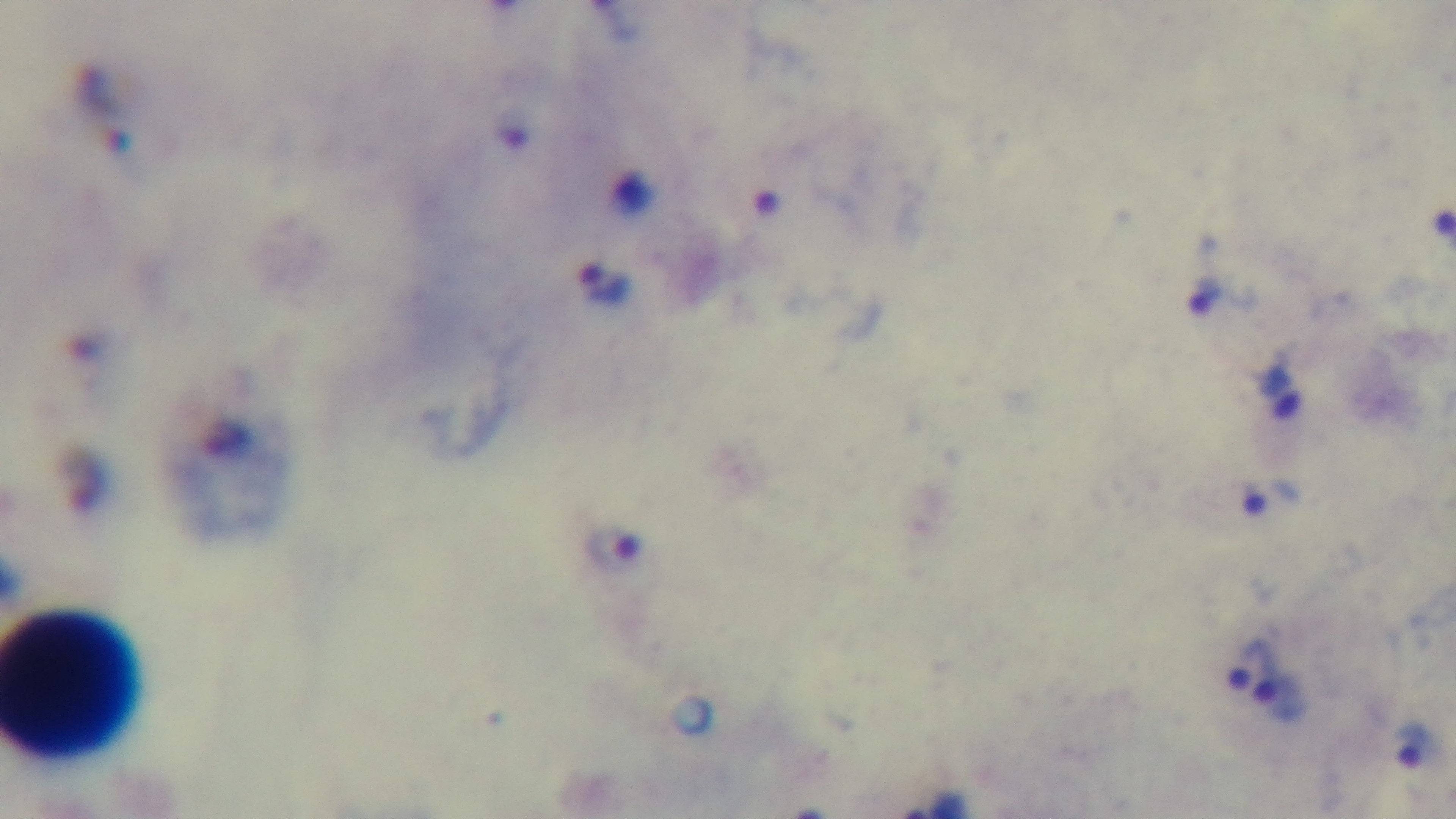
preparation = thick
modality = light microscopy
stain = Giemsa
capture = mounted 4K digital camera
malaria status = infected
field of view = single
objective = 100x oil immersion